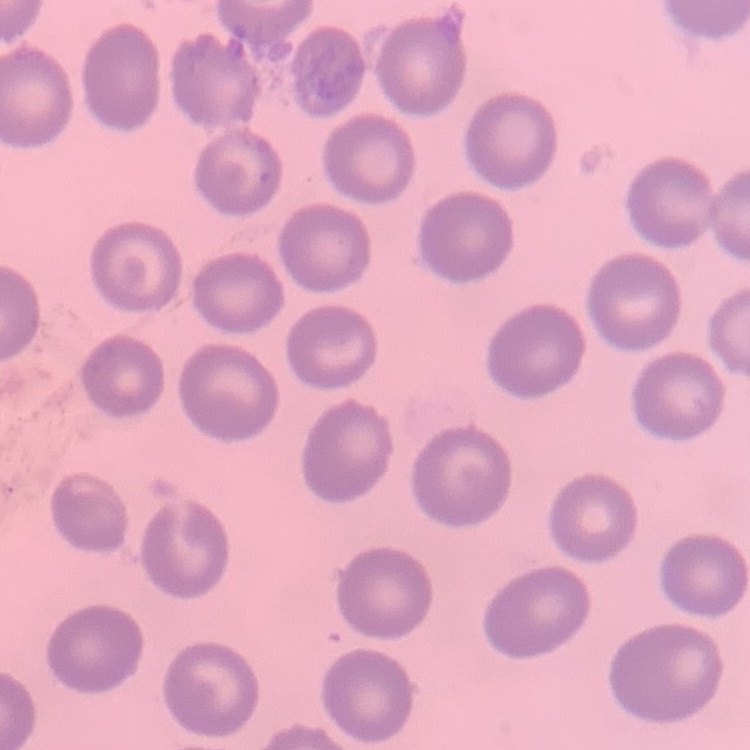
The erythrocytes exhibit no rouleaux formation. Thin blood film. Square crop of a larger photomicrograph. Stained with either Field's or Giemsa.